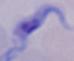

modality = photomicrograph
magnification = 1000x
identification = trypanosome